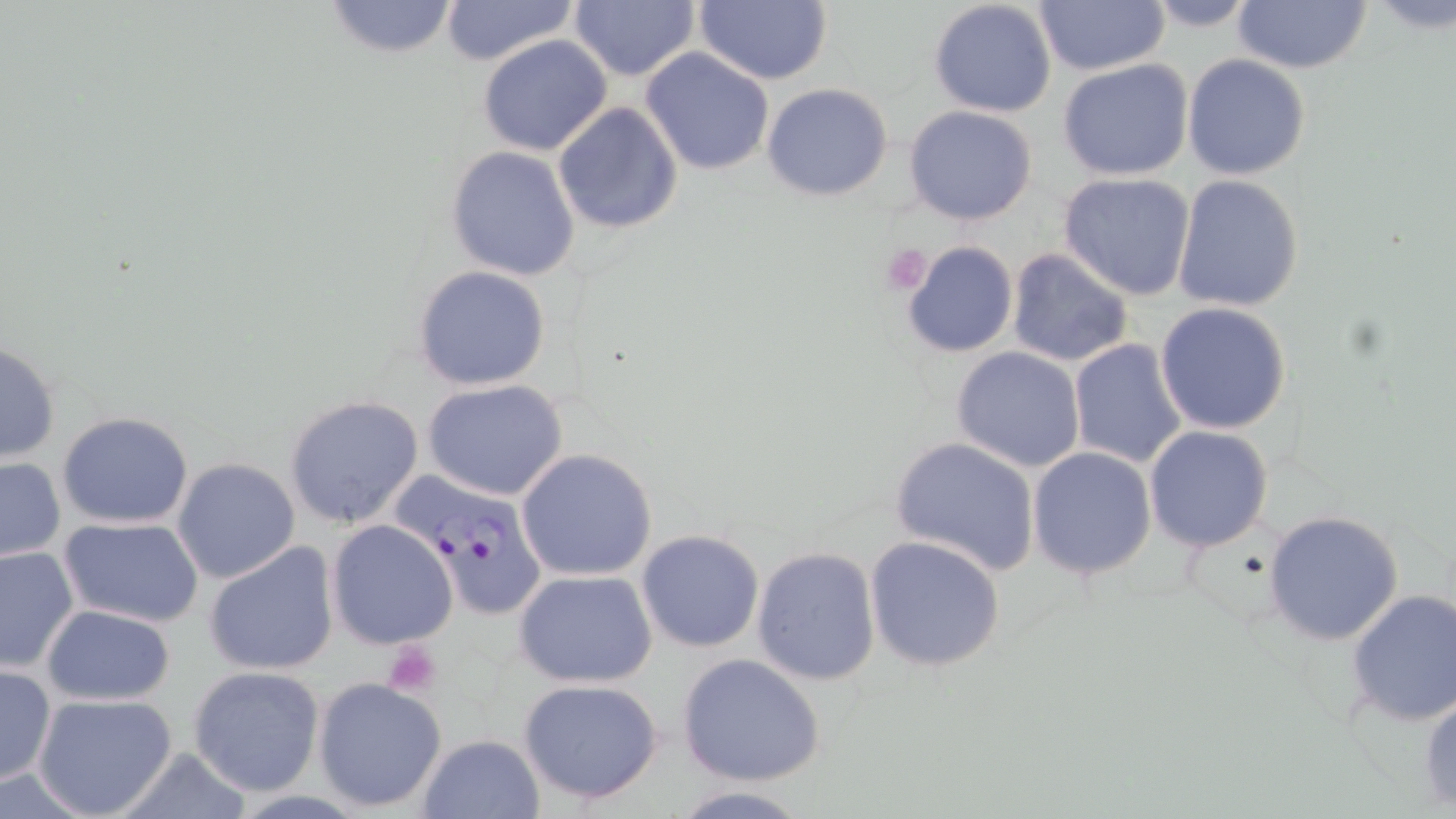
Approximate bounding boxes as (x1, y1, x2, y2) in pixels. Platelet locations: (878, 242, 934, 296), (390, 646, 441, 697). Plasmodium falciparum-infected red blood cell locations: (399, 470, 555, 618). Uninfected red blood cell locations: (322, 0, 461, 59), (438, 0, 579, 66), (693, 0, 833, 86), (928, 1, 1058, 117), (1140, 1, 1267, 31), (1233, 1, 1371, 74), (570, 2, 701, 81), (1034, 2, 1167, 76), (477, 36, 613, 156), (640, 46, 777, 175), (1182, 54, 1312, 180), (1057, 59, 1195, 181), (762, 83, 894, 201), (552, 102, 684, 235), (904, 105, 1038, 225), (445, 146, 580, 281), (1058, 172, 1198, 300), (1171, 174, 1305, 313), (899, 240, 1019, 357), (1005, 250, 1135, 367), (412, 264, 552, 391), (1155, 301, 1292, 433), (1067, 338, 1190, 470), (1, 339, 61, 464), (951, 345, 1087, 472), (424, 380, 569, 501), (283, 394, 423, 530), (58, 412, 196, 529), (1144, 425, 1275, 552), (889, 436, 1040, 577), (1026, 446, 1157, 579), (515, 448, 658, 581), (1, 455, 65, 562), (173, 457, 300, 584), (1263, 511, 1404, 646), (57, 515, 203, 628), (326, 520, 459, 650), (636, 530, 765, 652), (865, 534, 1004, 671), (205, 540, 340, 677), (1, 545, 78, 673), (751, 546, 882, 686), (513, 568, 659, 687), (1346, 589, 1456, 726), (40, 603, 177, 707), (677, 655, 824, 786), (0, 664, 55, 786), (187, 664, 329, 797), (313, 676, 447, 812), (517, 677, 665, 807), (1419, 688, 1456, 811), (32, 693, 178, 819), (415, 733, 547, 819), (665, 787, 816, 817). Slide-level diagnosis: Plasmodium falciparum. Single field of view. May-Grünwald-Giemsa-stained preparation. Light microscopy. Thin blood smear. Captured at 1000x magnification. Image is 1456×819 pixels.